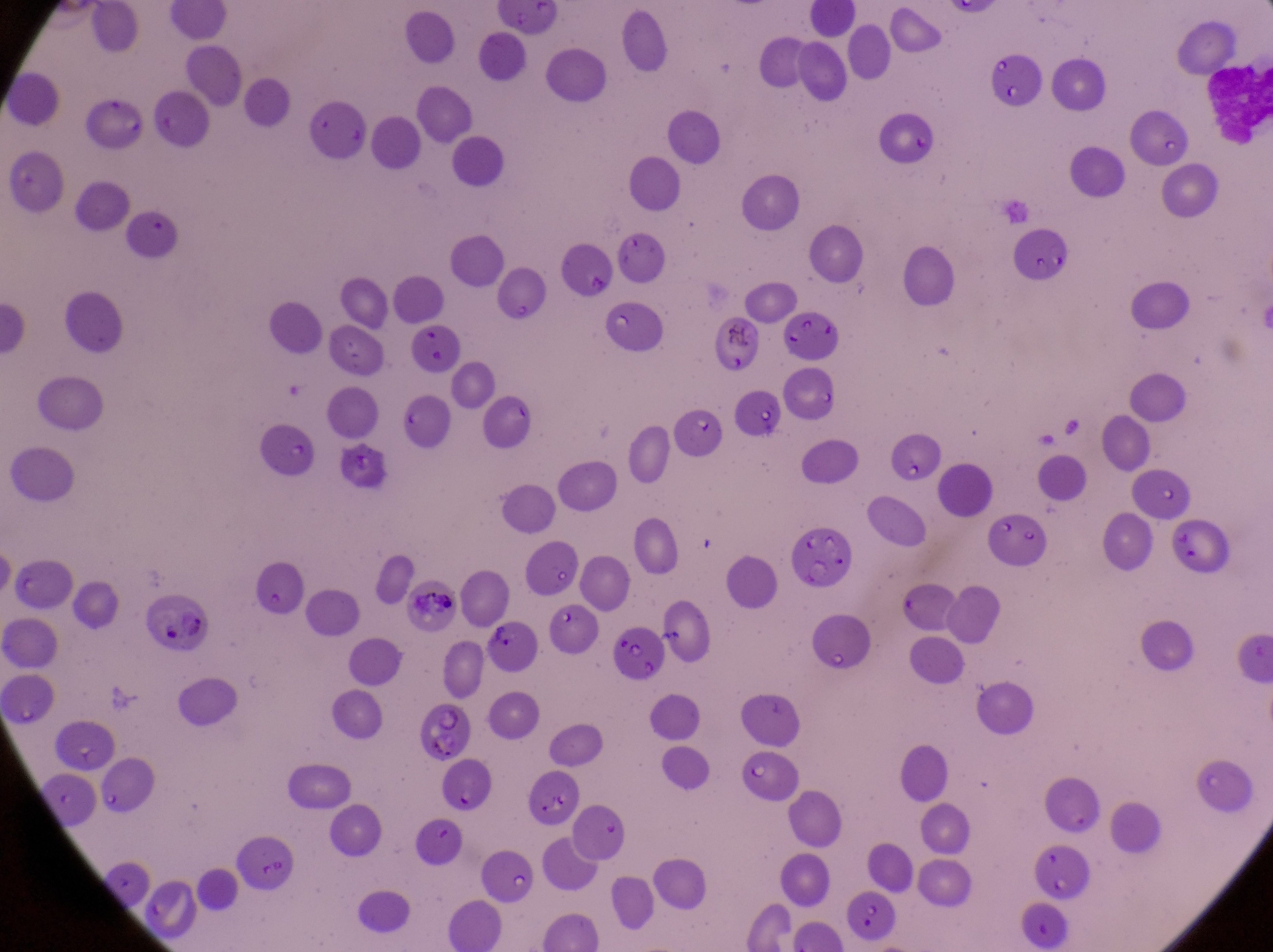 Approximate bounding boxes as [left, top, right, bottom] in pixels. Leukocyte locations: [1202, 57, 1268, 136]. Parasitised red blood cell locations: [1006, 220, 1075, 288], [148, 591, 220, 661], [484, 619, 544, 674], [424, 704, 479, 767]. Artifact (platelet-like body, stain precipitate, or debris) locations: [711, 312, 759, 354], [337, 445, 387, 487], [407, 579, 460, 634]. Magnification of 1000x. Photographed through the eyepiece of an Olympus CX-23 microscope with a smartphone camera. Thin blood film. Image is 1273×952 pixels. Single field of view. Collected in Uganda.